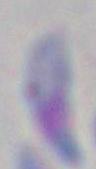

Summary:
  - Modality: photomicrograph
  - Identification: Toxoplasma gondii
  - Magnification: 1000x